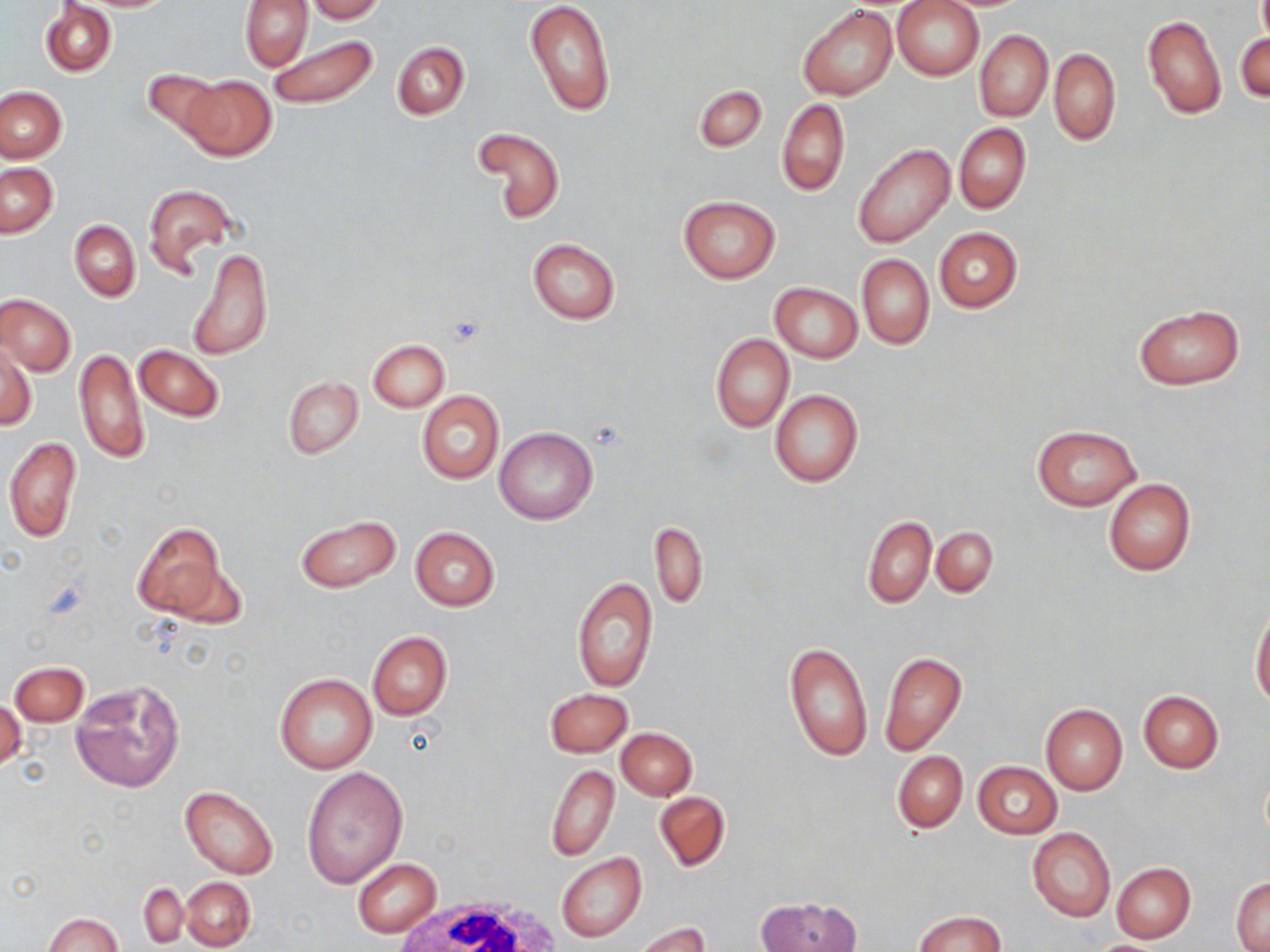
Summary:
  - Coordinate format: approximate bounding boxes as (x1,y1)-(x2,y2) corner pairs in pixels
  - White blood cell locations: (387,894)-(563,952)
  - Uninfected red blood cell locations: (239,0)-(312,70), (305,0)-(385,22), (523,0)-(615,116), (892,0)-(984,80), (40,2)-(116,76), (797,5)-(898,100), (1142,15)-(1225,120), (975,30)-(1053,121), (1236,32)-(1270,103), (267,34)-(378,110), (392,41)-(469,120), (1050,49)-(1120,145), (142,68)-(225,141), (180,74)-(275,161), (694,84)-(767,152), (0,87)-(66,162), (777,99)-(850,196), (953,122)-(1031,214), (475,127)-(566,224), (853,142)-(956,249), (1,163)-(58,237), (142,183)-(238,275), (678,196)-(779,283), (69,219)-(140,301), (934,227)-(1023,312), (527,239)-(621,324), (189,246)-(273,362), (857,254)-(934,349), (770,282)-(862,362), (1,293)-(75,375), (1132,305)-(1245,390), (710,333)-(794,432), (368,339)-(449,411), (2,343)-(36,432), (134,344)-(225,422), (74,347)-(148,464), (283,376)-(363,459), (770,390)-(864,488), (417,392)-(504,484), (1031,424)-(1142,510), (494,427)-(599,525), (3,436)-(82,544), (1103,480)-(1195,575), (294,513)-(401,594), (862,516)-(935,607), (650,521)-(707,610), (131,522)-(230,622), (932,526)-(998,596), (409,527)-(499,611), (572,576)-(658,692), (1251,606)-(1270,711), (367,631)-(452,721), (782,641)-(873,763), (879,651)-(967,755), (10,662)-(88,726), (274,674)-(377,775), (71,679)-(185,793), (543,687)-(634,757), (1138,690)-(1223,772), (1,698)-(25,776), (1041,703)-(1127,794), (615,727)-(696,801), (893,751)-(967,832), (973,760)-(1062,839), (545,764)-(620,861), (301,766)-(408,889), (180,784)-(280,879), (654,791)-(731,872), (1027,828)-(1116,922), (556,852)-(646,942), (353,858)-(442,937), (1111,862)-(1196,943), (180,876)-(255,949), (1230,876)-(1270,951), (140,883)-(187,946), (758,896)-(861,952), (913,911)-(1008,952), (44,913)-(122,952), (633,921)-(710,952)
  - Slide-level diagnosis: negative for blood parasites
  - Magnification: 1000x
  - Preparation: thin blood smear
  - Image size: 1270×952 pixels
  - Stain: May-Grünwald-Giemsa
  - Field of view: one of a larger specimen
  - Modality: optical microscopy